Outline each Plasmodium ovale-infected red blood cell.
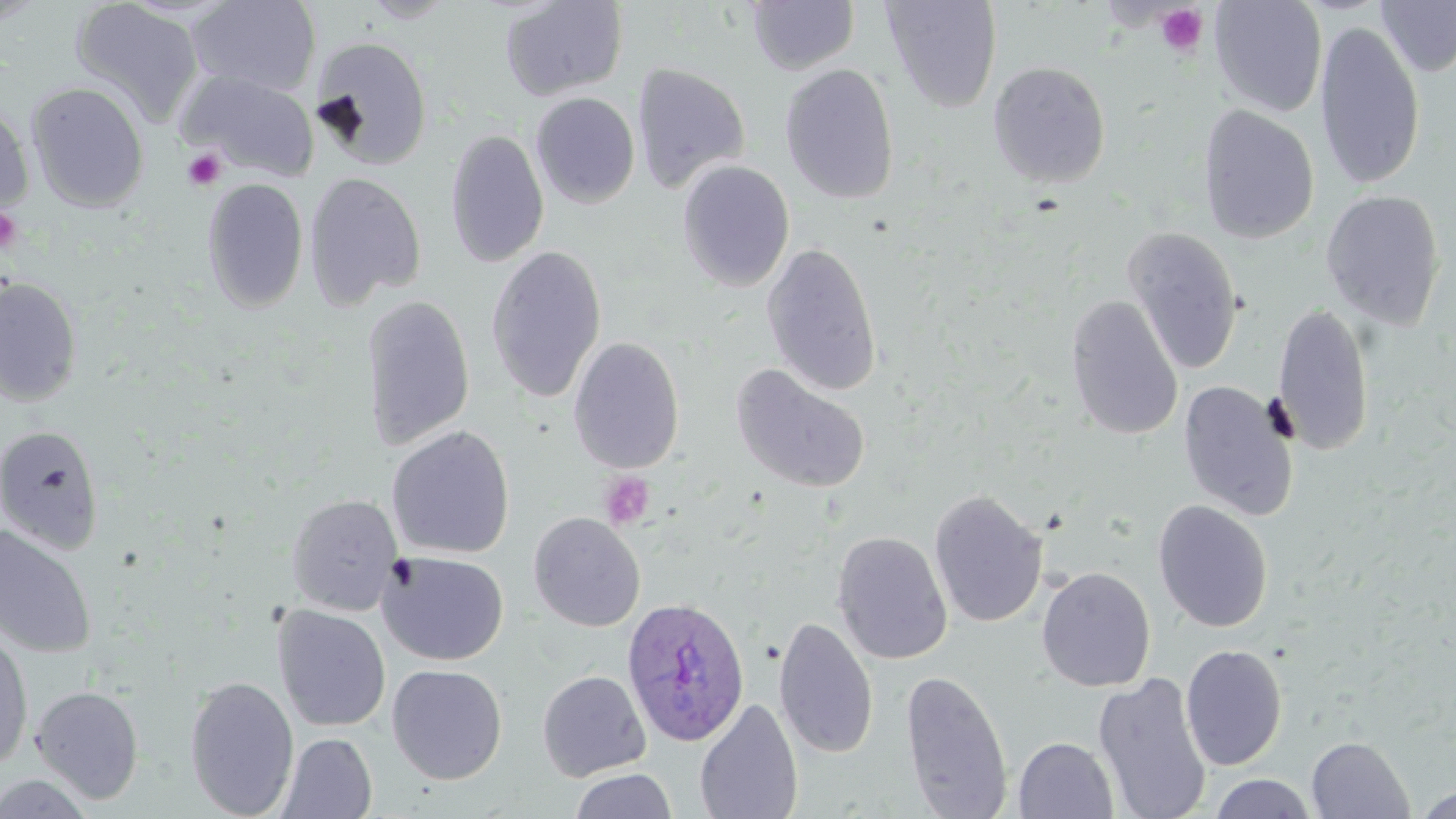

Approximate bounding boxes as (x1, y1, x2, y2) in pixels.
Plasmodium ovale-infected red blood cells: (621, 596, 750, 747).

Uninfected red blood cell locations: (186, 0, 322, 98), (360, 0, 459, 24), (500, 0, 629, 100), (881, 0, 1003, 113), (1210, 0, 1328, 117), (1376, 0, 1456, 77), (69, 1, 204, 125), (746, 1, 860, 75), (1314, 21, 1425, 190), (310, 35, 434, 170), (989, 61, 1111, 188), (631, 63, 751, 195), (779, 63, 900, 205), (180, 71, 320, 181), (27, 82, 149, 212), (530, 92, 641, 209), (0, 100, 34, 218), (1198, 105, 1320, 245), (445, 129, 549, 268), (676, 160, 795, 292), (304, 171, 427, 309), (202, 177, 309, 314), (1320, 189, 1446, 330), (1121, 226, 1244, 375), (761, 241, 883, 398), (485, 245, 607, 404), (0, 277, 82, 407), (361, 294, 476, 451), (1064, 296, 1183, 440), (1271, 301, 1376, 456), (568, 337, 685, 474), (730, 364, 871, 494), (1177, 380, 1300, 520), (0, 425, 105, 555), (386, 425, 515, 559), (928, 488, 1049, 630), (286, 494, 402, 615), (1153, 499, 1273, 633), (528, 512, 646, 631), (0, 522, 97, 658), (831, 530, 953, 664), (378, 551, 509, 666), (1037, 566, 1156, 693), (273, 605, 391, 732), (773, 615, 879, 760), (0, 630, 34, 772), (1180, 644, 1287, 771), (386, 664, 508, 784), (899, 669, 1014, 818), (537, 670, 651, 781), (1092, 671, 1212, 819), (185, 675, 299, 818), (31, 685, 144, 804), (694, 698, 804, 819), (276, 732, 377, 818), (1013, 736, 1119, 819), (1306, 736, 1415, 818), (568, 769, 678, 819), (0, 772, 96, 818), (1207, 774, 1318, 818), (1414, 787, 1455, 819). Platelet locations: (1154, 4, 1209, 57), (182, 148, 227, 192), (0, 206, 23, 255), (599, 471, 656, 529). Slide-level diagnosis: Plasmodium ovale. Thin blood film. 1000x magnification. Single field of view. May-Grünwald-Giemsa stain. Image is 1456×819 pixels. Optical microscopy.